Classify this cell by malaria status.
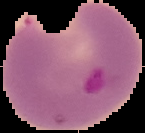

Parasitized.

Image is 145×133 pixels. Cell region segmented out of the field of view; the surrounding area is masked to black. From a thin blood smear.